Assess this cell for malaria.
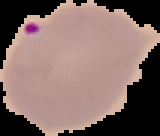
Parasitized.

From a thin blood smear. Cell region segmented out of the field of view; the surrounding area is masked to black. Image is 160×136 pixels.